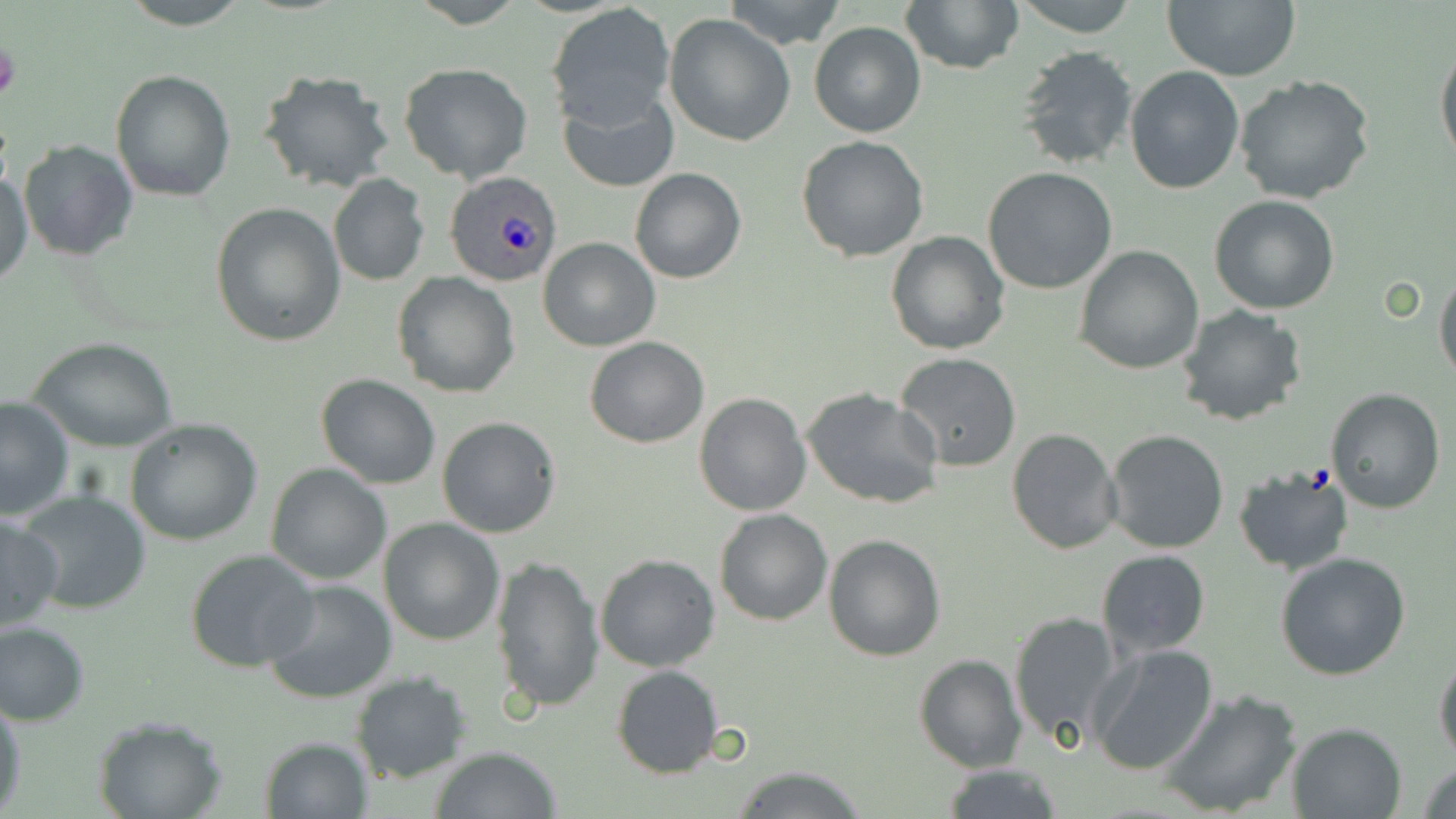
{
  "slide_level_diagnosis": "Plasmodium ovale",
  "stain": "May-Grünwald-Giemsa",
  "preparation": "thin blood film",
  "magnification": "1000x",
  "field_of_view": "one of a larger specimen",
  "image_size": "1456×819 pixels",
  "platelet_locations": "approximate bounding boxes as named x1/y1/x2/y2 corners in pixels: (x1=0, y1=40, x2=21, y2=105)",
  "modality": "light microscopy",
  "uninfected_red_blood_cell_locations": "approximate bounding boxes as named x1/y1/x2/y2 corners in pixels: (x1=115, y1=0, x2=254, y2=29), (x1=722, y1=0, x2=848, y2=50), (x1=1015, y1=0, x2=1138, y2=37), (x1=1160, y1=0, x2=1301, y2=82), (x1=901, y1=1, x2=1023, y2=76), (x1=547, y1=4, x2=676, y2=129), (x1=663, y1=13, x2=796, y2=147), (x1=808, y1=20, x2=926, y2=138), (x1=1436, y1=35, x2=1456, y2=172), (x1=1015, y1=45, x2=1140, y2=172), (x1=398, y1=62, x2=533, y2=183), (x1=1125, y1=66, x2=1246, y2=194), (x1=110, y1=68, x2=237, y2=201), (x1=256, y1=69, x2=395, y2=194), (x1=1234, y1=76, x2=1376, y2=207), (x1=559, y1=91, x2=679, y2=194), (x1=796, y1=135, x2=931, y2=261), (x1=17, y1=139, x2=140, y2=261), (x1=629, y1=166, x2=746, y2=284), (x1=0, y1=167, x2=33, y2=288), (x1=982, y1=168, x2=1117, y2=295), (x1=328, y1=173, x2=429, y2=286), (x1=1209, y1=195, x2=1340, y2=315), (x1=211, y1=203, x2=345, y2=346), (x1=885, y1=231, x2=1010, y2=355), (x1=540, y1=237, x2=660, y2=352), (x1=1073, y1=244, x2=1203, y2=374), (x1=1434, y1=269, x2=1456, y2=384), (x1=392, y1=273, x2=521, y2=398), (x1=1177, y1=305, x2=1309, y2=427), (x1=28, y1=336, x2=180, y2=453), (x1=585, y1=337, x2=710, y2=448), (x1=894, y1=353, x2=1023, y2=473), (x1=315, y1=374, x2=442, y2=490), (x1=801, y1=385, x2=944, y2=510), (x1=1325, y1=388, x2=1446, y2=512), (x1=694, y1=392, x2=811, y2=516), (x1=0, y1=397, x2=75, y2=520), (x1=437, y1=416, x2=561, y2=538), (x1=124, y1=417, x2=263, y2=546), (x1=1007, y1=427, x2=1121, y2=553), (x1=1104, y1=429, x2=1230, y2=553), (x1=265, y1=463, x2=392, y2=585), (x1=1233, y1=465, x2=1355, y2=575), (x1=17, y1=489, x2=151, y2=616), (x1=714, y1=508, x2=833, y2=626), (x1=0, y1=515, x2=66, y2=632), (x1=378, y1=517, x2=505, y2=645), (x1=824, y1=534, x2=946, y2=661), (x1=1096, y1=548, x2=1211, y2=657), (x1=184, y1=549, x2=320, y2=673), (x1=595, y1=553, x2=720, y2=672), (x1=1275, y1=553, x2=1411, y2=682), (x1=491, y1=555, x2=605, y2=716), (x1=262, y1=579, x2=399, y2=704), (x1=1008, y1=610, x2=1123, y2=748), (x1=0, y1=620, x2=91, y2=726), (x1=1087, y1=644, x2=1219, y2=775), (x1=1434, y1=653, x2=1456, y2=765), (x1=914, y1=654, x2=1025, y2=772), (x1=611, y1=665, x2=724, y2=778), (x1=349, y1=671, x2=472, y2=784), (x1=1157, y1=688, x2=1302, y2=817), (x1=0, y1=692, x2=24, y2=814), (x1=93, y1=715, x2=228, y2=819), (x1=1285, y1=722, x2=1408, y2=818), (x1=258, y1=736, x2=371, y2=817), (x1=429, y1=745, x2=564, y2=819), (x1=1418, y1=760, x2=1456, y2=819), (x1=938, y1=763, x2=1062, y2=819), (x1=730, y1=766, x2=869, y2=819)",
  "plasmodium_ovale_infected_red_blood_cell_locations": "approximate bounding boxes as named x1/y1/x2/y2 corners in pixels: (x1=445, y1=170, x2=563, y2=287)"
}